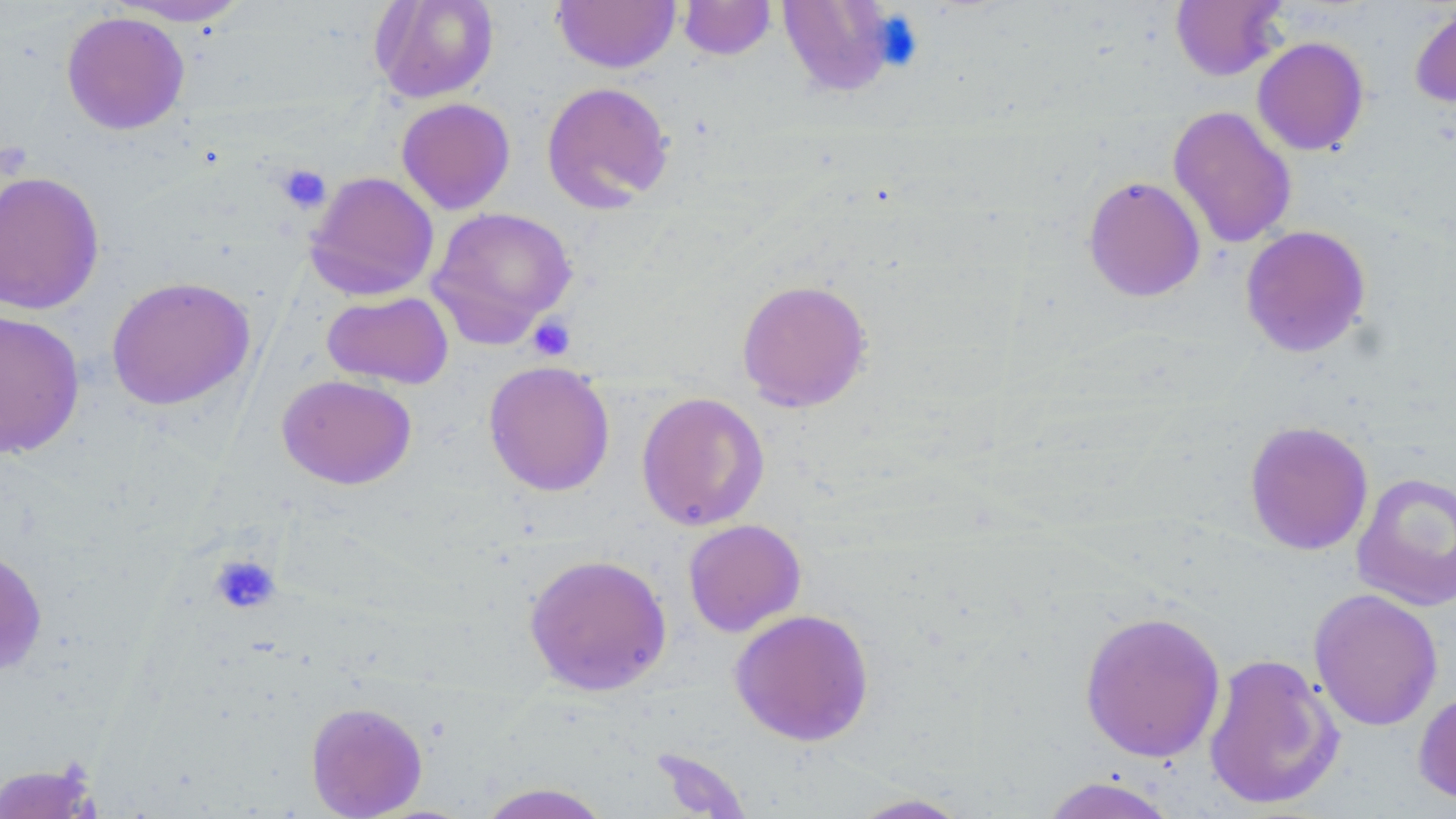
slide-level diagnosis = no evidence of blood parasites
preparation = thin blood film
modality = optical microscopy
field of view = single
platelet locations = approximate bounding boxes as named x1/y1/x2/y2 corners in pixels: (x1=275, y1=163, x2=331, y2=215), (x1=527, y1=314, x2=576, y2=361), (x1=210, y1=554, x2=281, y2=615)
stain = May-Grünwald-Giemsa
magnification = 1000x
image size = 1456×819 pixels
uninfected red blood cell locations = approximate bounding boxes as named x1/y1/x2/y2 corners in pixels: (x1=107, y1=0, x2=254, y2=26), (x1=371, y1=0, x2=500, y2=103), (x1=778, y1=0, x2=898, y2=97), (x1=1170, y1=0, x2=1288, y2=81), (x1=552, y1=1, x2=680, y2=73), (x1=677, y1=1, x2=776, y2=60), (x1=1410, y1=3, x2=1456, y2=109), (x1=61, y1=11, x2=190, y2=135), (x1=1252, y1=36, x2=1369, y2=156), (x1=541, y1=81, x2=675, y2=212), (x1=396, y1=97, x2=516, y2=215), (x1=1168, y1=105, x2=1297, y2=249), (x1=0, y1=170, x2=105, y2=315), (x1=305, y1=171, x2=439, y2=301), (x1=1082, y1=176, x2=1206, y2=302), (x1=427, y1=206, x2=578, y2=347), (x1=1240, y1=225, x2=1371, y2=358), (x1=106, y1=276, x2=255, y2=411), (x1=735, y1=278, x2=873, y2=412), (x1=322, y1=291, x2=454, y2=390), (x1=0, y1=310, x2=85, y2=459), (x1=483, y1=360, x2=615, y2=497), (x1=277, y1=374, x2=417, y2=490), (x1=635, y1=391, x2=770, y2=531), (x1=1244, y1=420, x2=1374, y2=555), (x1=1351, y1=471, x2=1456, y2=611), (x1=683, y1=519, x2=806, y2=637), (x1=0, y1=546, x2=47, y2=676), (x1=524, y1=553, x2=672, y2=696), (x1=1308, y1=588, x2=1443, y2=732), (x1=729, y1=608, x2=874, y2=746), (x1=1079, y1=609, x2=1227, y2=763), (x1=1202, y1=652, x2=1345, y2=811), (x1=1414, y1=687, x2=1456, y2=807), (x1=305, y1=701, x2=428, y2=818), (x1=0, y1=761, x2=102, y2=819), (x1=1037, y1=775, x2=1181, y2=818), (x1=476, y1=782, x2=614, y2=819), (x1=846, y1=792, x2=975, y2=818)